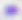 400x magnification. Micrograph. Toxoplasma gondii is shown.